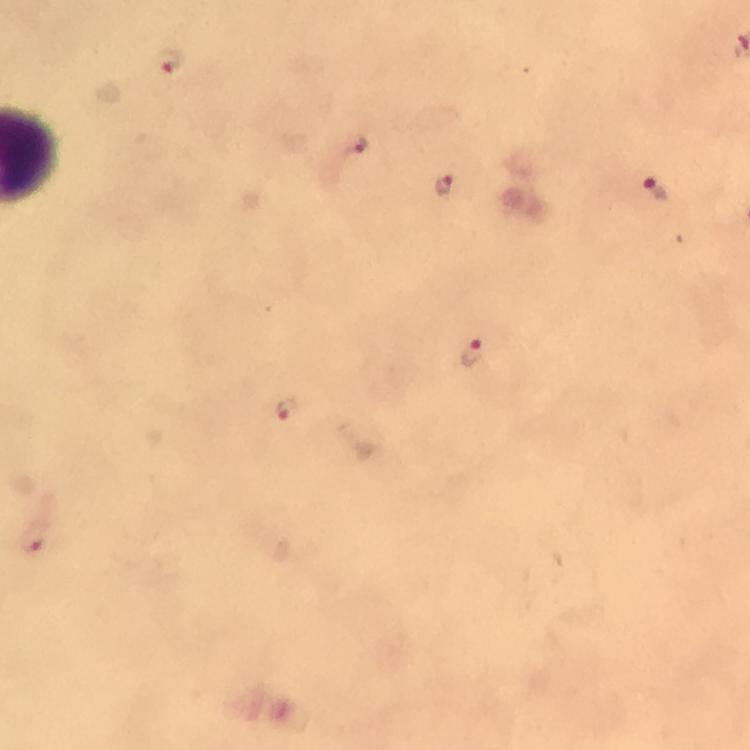

Approximate object centers, in pixels from the top-left corner.
Summary:
  - Malaria parasite locations: (x=171, y=62), (x=358, y=143), (x=443, y=184), (x=654, y=189), (x=473, y=352), (x=286, y=409), (x=33, y=540)
  - Context: from a diagnostic examination for malaria
  - Stain: Giemsa
  - Immersion oil: applied
  - Magnification: 100x
  - Cropped from: one field of view
  - Image size: 750×750 pixels
  - Capture: smartphone photograph through a microscope
  - Preparation: thick blood film